Identify the parasite.
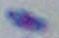
This is Toxoplasma gondii.

modality: micrograph
magnification: 1000x